State which cell type is depicted.
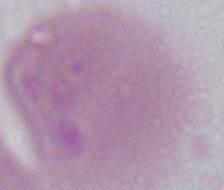
This is an erythrocyte.

Micrograph. Captured at 1000x magnification.